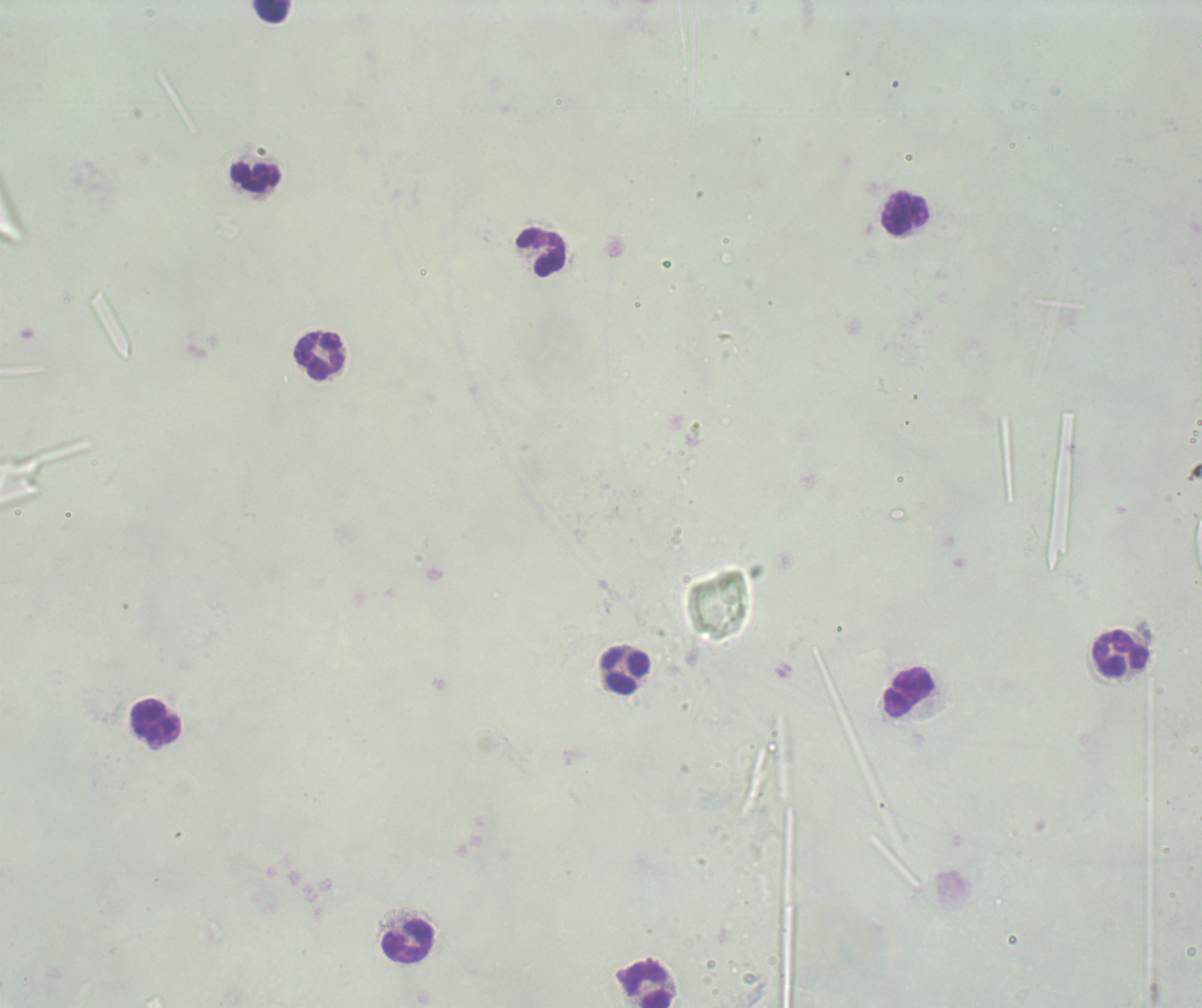

Approximate centers as [x, y] in pixels.
Summary:
  - Leukocyte locations: [272, 11], [256, 178], [905, 213], [542, 253], [320, 356], [1122, 654], [625, 671], [910, 692], [156, 722], [408, 941], [648, 985]
  - Result: negative for malaria parasites
  - Background quality: poor
  - Field of view: single
  - Stain: Romanowsky
  - Context: previously used in an actual diagnosis
  - Magnification: 100x
  - Image size: 1202×1008 pixels
  - Preparation: thick blood smear